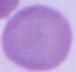

A red blood cell is seen. 1000x magnification. Photomicrograph.